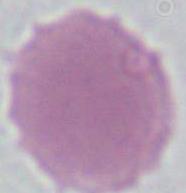

Captured at 1000x magnification. Micrograph. An erythrocyte is shown.